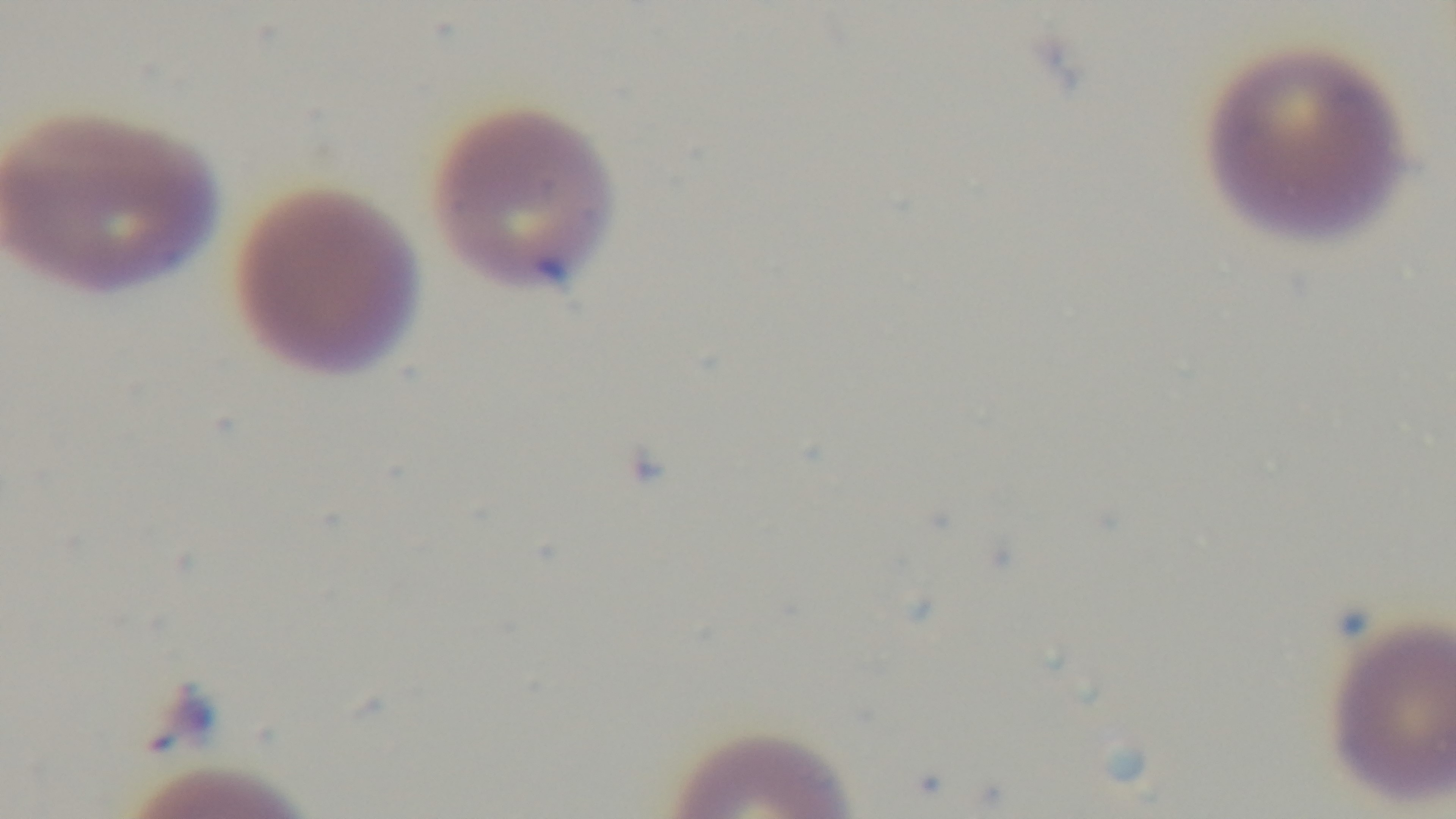

{
  "capture": "mounted 4K digital camera",
  "malaria_status": "infected",
  "modality": "light microscopy",
  "preparation": "thin blood film",
  "field_of_view": "single",
  "stain": "Giemsa",
  "objective": "100x oil immersion"
}